Report the malaria status of this cell.
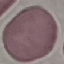
Uninfected.

{
  "preparation": "thin smear",
  "image_type": "automatically extracted cell patch, resized to 64 × 64 pixels",
  "capture": "smartphone camera at the microscope eyepiece",
  "stain": "Giemsa"
}